Report the malaria status of this cell.
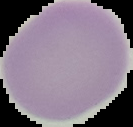

It is uninfected.

Summary:
  - Preparation: thin blood smear
  - Image size: 133×127 pixels
  - Image type: segmented cell region on a black background